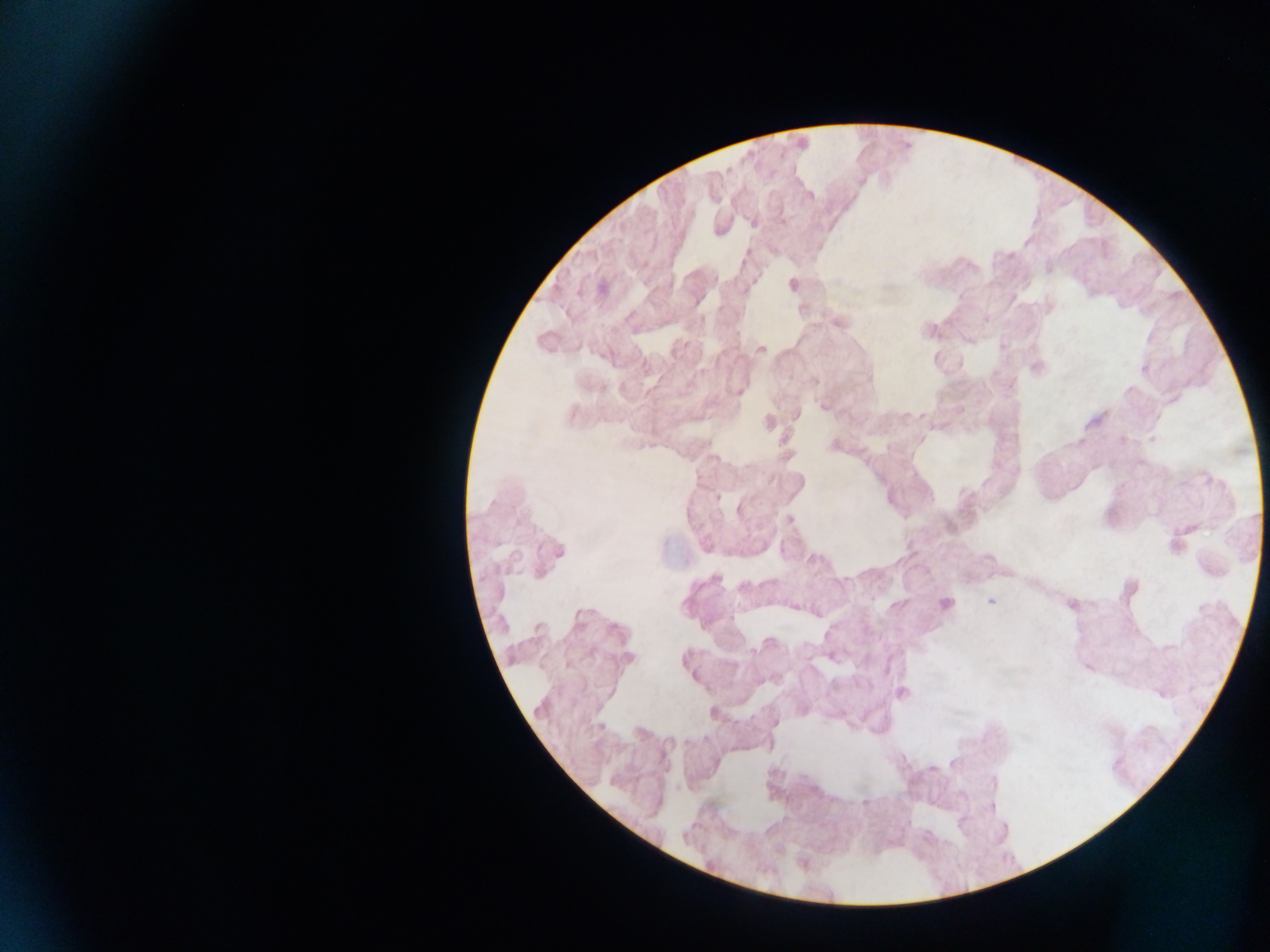

Approximate centers as [x, y] in pixels. Plasmodium parasite locations: [809, 195], [782, 220], [753, 221], [793, 284], [838, 321], [967, 338], [760, 349], [1035, 367], [738, 391], [824, 406], [795, 414], [768, 423], [1153, 439], [788, 519], [1176, 543], [554, 553], [990, 600], [944, 604], [1070, 604], [794, 607], [628, 658], [1089, 667], [901, 692], [773, 723]. Mobile-phone photograph taken through the microscope. Collected in Ghana. Thick blood smear. Image is 1270×952 pixels. One field of view.